Give a bounding box for every Plasmodium parasite.
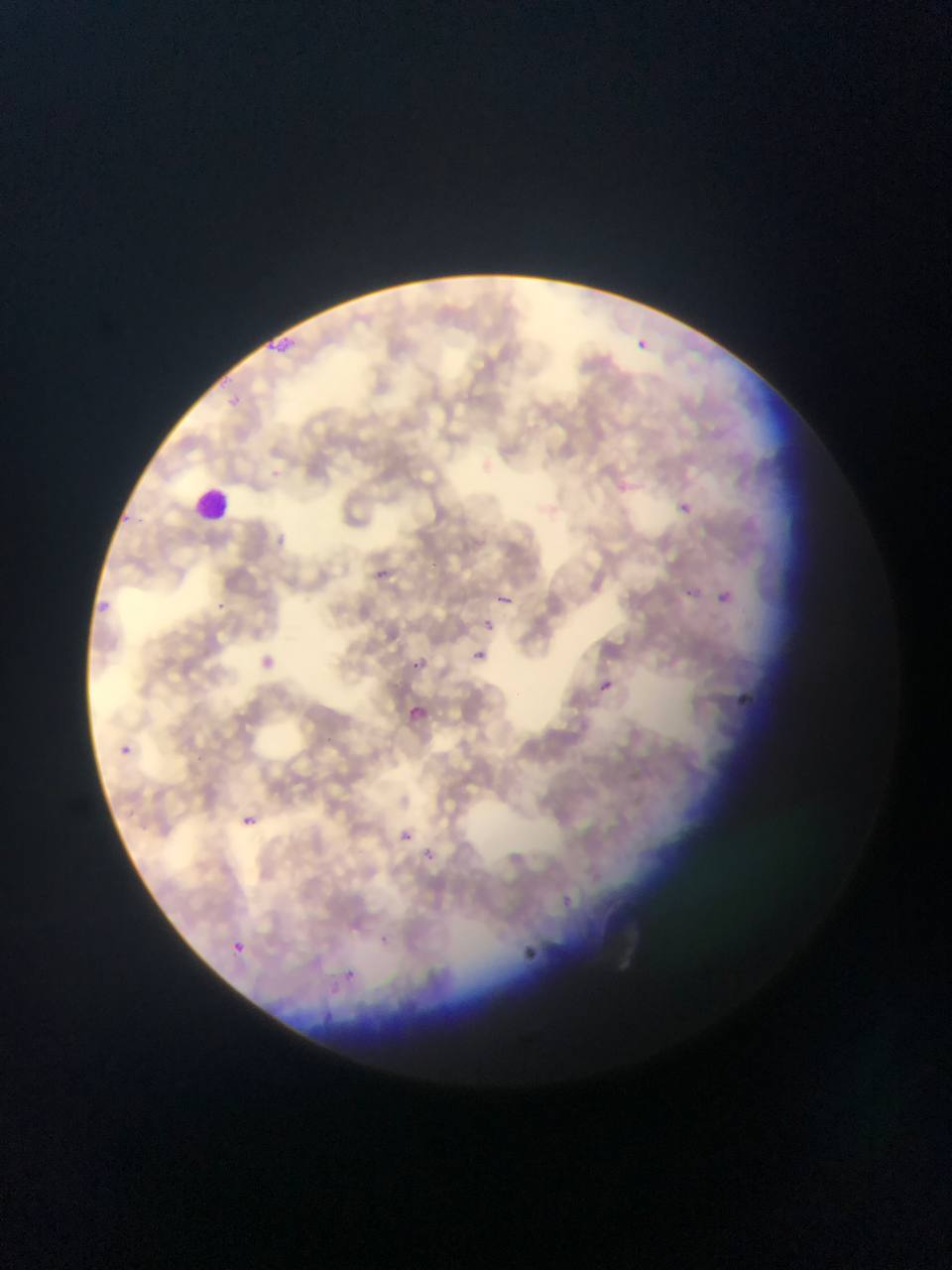

Approximate bounding boxes as [left, top, right, bottom] in pixels.
Plasmodium parasites: [626, 323, 666, 369], [260, 327, 318, 364], [611, 479, 630, 497], [677, 497, 698, 516], [361, 558, 417, 585], [714, 580, 738, 608], [493, 584, 530, 617], [84, 586, 121, 619], [470, 648, 489, 665], [252, 650, 281, 676], [407, 657, 429, 676], [596, 679, 616, 697], [733, 685, 763, 712], [401, 702, 434, 732], [115, 742, 135, 760], [238, 813, 260, 831], [396, 826, 416, 846], [418, 844, 441, 866], [525, 934, 555, 964], [224, 938, 249, 959], [336, 956, 354, 980].

Summary:
  - Leukocyte locations: [188, 482, 236, 529]
  - Image size: 952×1270 pixels
  - Field of view: single
  - Country: Ghana
  - Preparation: thin blood smear
  - Capture: mobile-phone photograph through a microscope